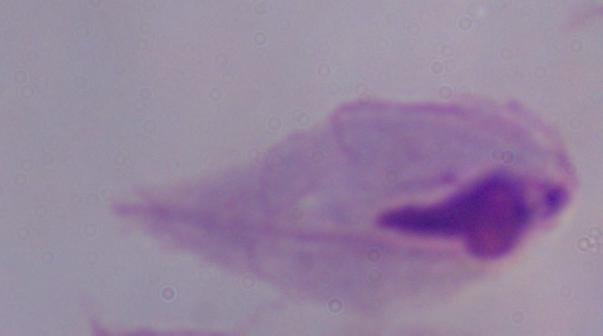
Summary:
  - Identification: trichomonad
  - Magnification: 1000x
  - Modality: photomicrograph